Identify the blood parasite species.
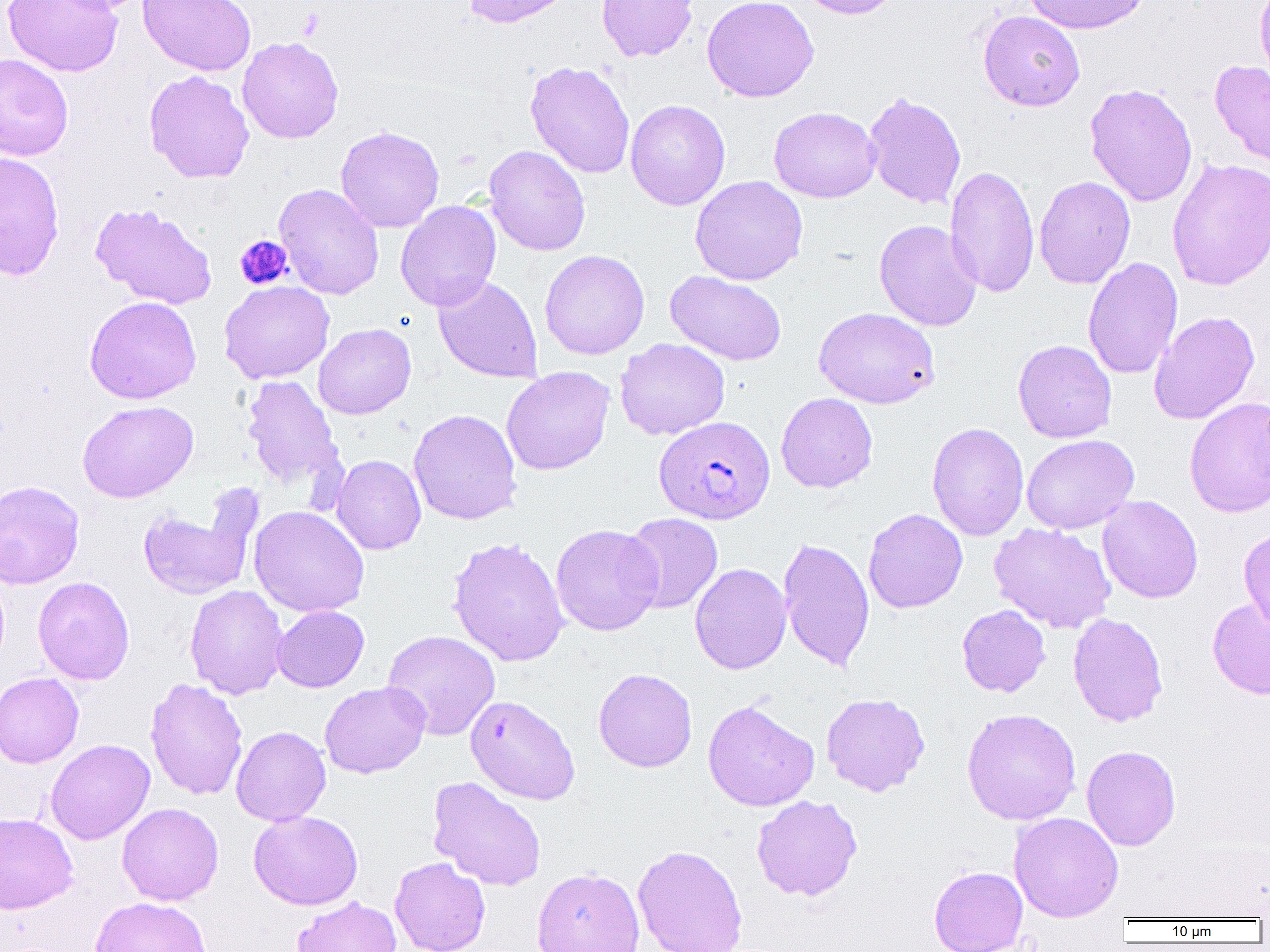

Plasmodium falciparum.

Approximate bounding boxes as [x1, y1, x2, y2] in pixels. Uninfected red blood cell locations: [2, 0, 124, 77], [137, 0, 256, 77], [462, 0, 576, 28], [596, 0, 698, 62], [702, 0, 819, 103], [795, 0, 906, 19], [1024, 0, 1148, 34], [1255, 0, 1270, 88], [978, 10, 1086, 111], [237, 36, 344, 144], [0, 53, 74, 161], [1209, 59, 1270, 168], [525, 61, 635, 178], [144, 70, 254, 183], [1084, 82, 1197, 207], [863, 92, 966, 209], [625, 99, 730, 211], [768, 106, 881, 203], [336, 125, 444, 233], [484, 145, 591, 256], [0, 152, 65, 281], [1166, 156, 1270, 291], [945, 165, 1039, 298], [690, 175, 808, 285], [1034, 176, 1136, 289], [274, 183, 384, 300], [395, 200, 501, 311], [89, 203, 218, 309], [874, 220, 982, 331], [540, 249, 650, 359], [1083, 257, 1183, 381], [665, 270, 788, 366], [433, 275, 543, 383], [219, 280, 334, 383], [84, 296, 202, 403], [814, 307, 939, 409], [1149, 311, 1260, 424], [313, 323, 416, 419], [615, 338, 730, 440], [1012, 339, 1117, 443], [501, 366, 615, 475], [241, 375, 343, 492], [776, 392, 878, 493], [1185, 396, 1270, 517], [77, 400, 198, 503], [408, 408, 522, 525], [927, 422, 1029, 541], [1021, 434, 1139, 534], [331, 454, 426, 555], [0, 480, 85, 589], [1097, 495, 1203, 603], [137, 502, 256, 599], [249, 506, 369, 617], [863, 508, 967, 614], [621, 513, 723, 614], [989, 523, 1116, 632], [550, 524, 664, 636], [1239, 528, 1270, 634], [447, 536, 570, 667], [778, 537, 875, 672], [689, 563, 792, 675], [33, 576, 134, 685], [185, 585, 288, 699], [1207, 598, 1270, 699], [957, 604, 1050, 697], [272, 605, 369, 692], [1068, 612, 1168, 727], [382, 629, 501, 741], [593, 668, 697, 773], [0, 672, 84, 768], [145, 678, 248, 800], [320, 681, 431, 778], [821, 692, 930, 796], [465, 694, 580, 805], [702, 700, 819, 811], [961, 708, 1081, 825], [231, 726, 331, 826], [45, 739, 155, 844], [1082, 745, 1181, 850], [427, 776, 547, 891], [751, 795, 862, 901], [117, 803, 224, 906], [248, 810, 363, 910], [1009, 812, 1123, 921], [0, 813, 78, 914], [632, 844, 748, 952], [389, 857, 490, 952], [929, 865, 1028, 952], [531, 866, 645, 952], [90, 896, 212, 952], [291, 896, 402, 952]. Platelet locations: [234, 234, 293, 290]. Plasmodium falciparum-infected red blood cell locations: [654, 415, 774, 524]. 1000x magnification. Image is 1270×952 pixels. Single field of view. Light microscopy. Thin blood smear.